Comment on the morphology of the red blood cells.
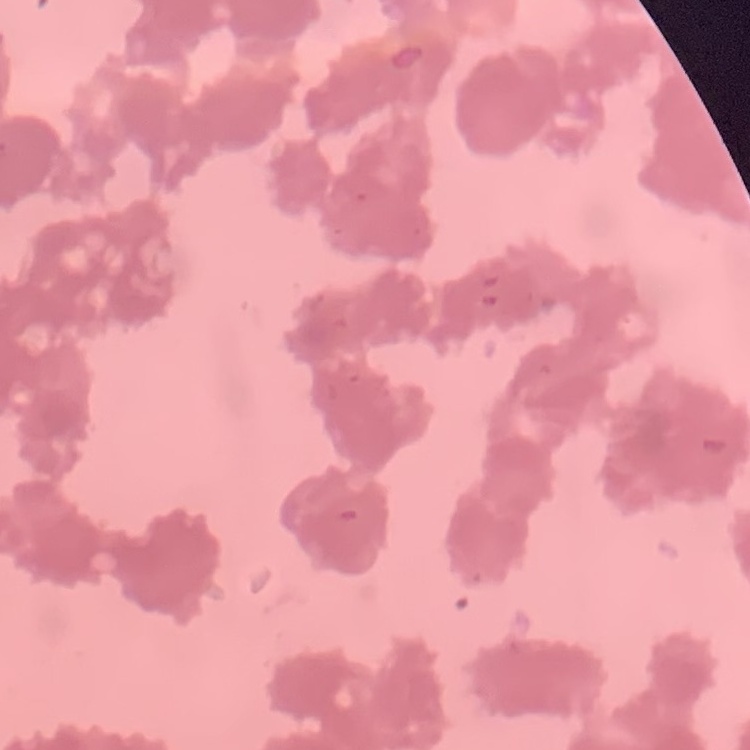

Rouleaux formation.

{
  "image_type": "one tile cut from a larger photomicrograph",
  "stain": "Field's or Giemsa",
  "preparation": "thin peripheral smear"
}